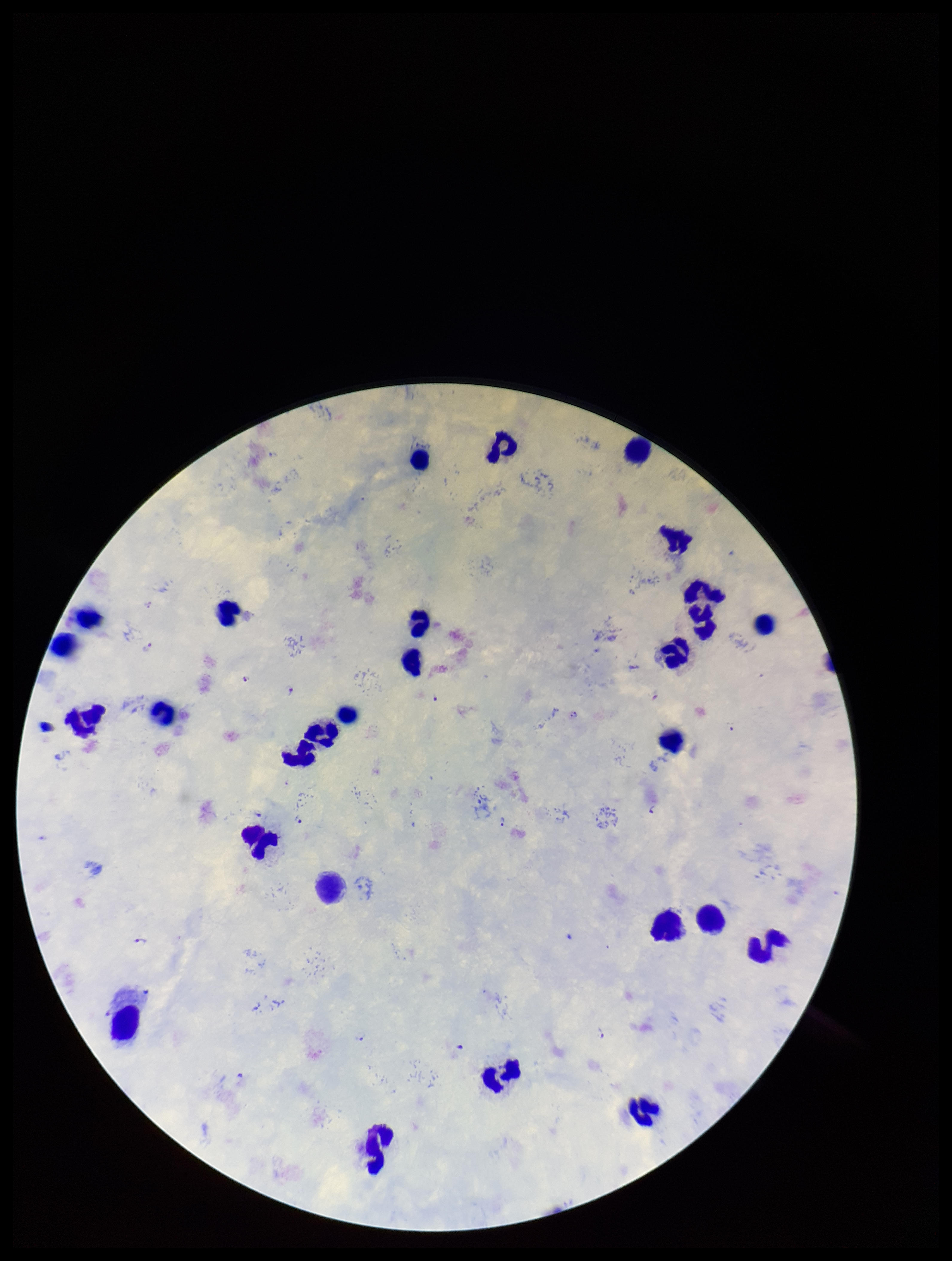

Species reported for this patient: Plasmodium falciparum. Preparation: thick smear. Smartphone photograph taken through the eyepiece of a microscope. One field from this slide. Patient malaria status: infected. Leukocyte count: 26. Image is 952×1261 pixels. Parasite count: 10. Plasmodium parasites: identified. Stained with Giemsa.